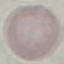 Result: negative for malaria parasites. Cell patch, automatically extracted from a larger field of view and resized to 64 × 64 pixels. Giemsa stain. Photographed with a smartphone camera at the microscope eyepiece. Thin blood smear.